Locate every Plasmodium parasite.
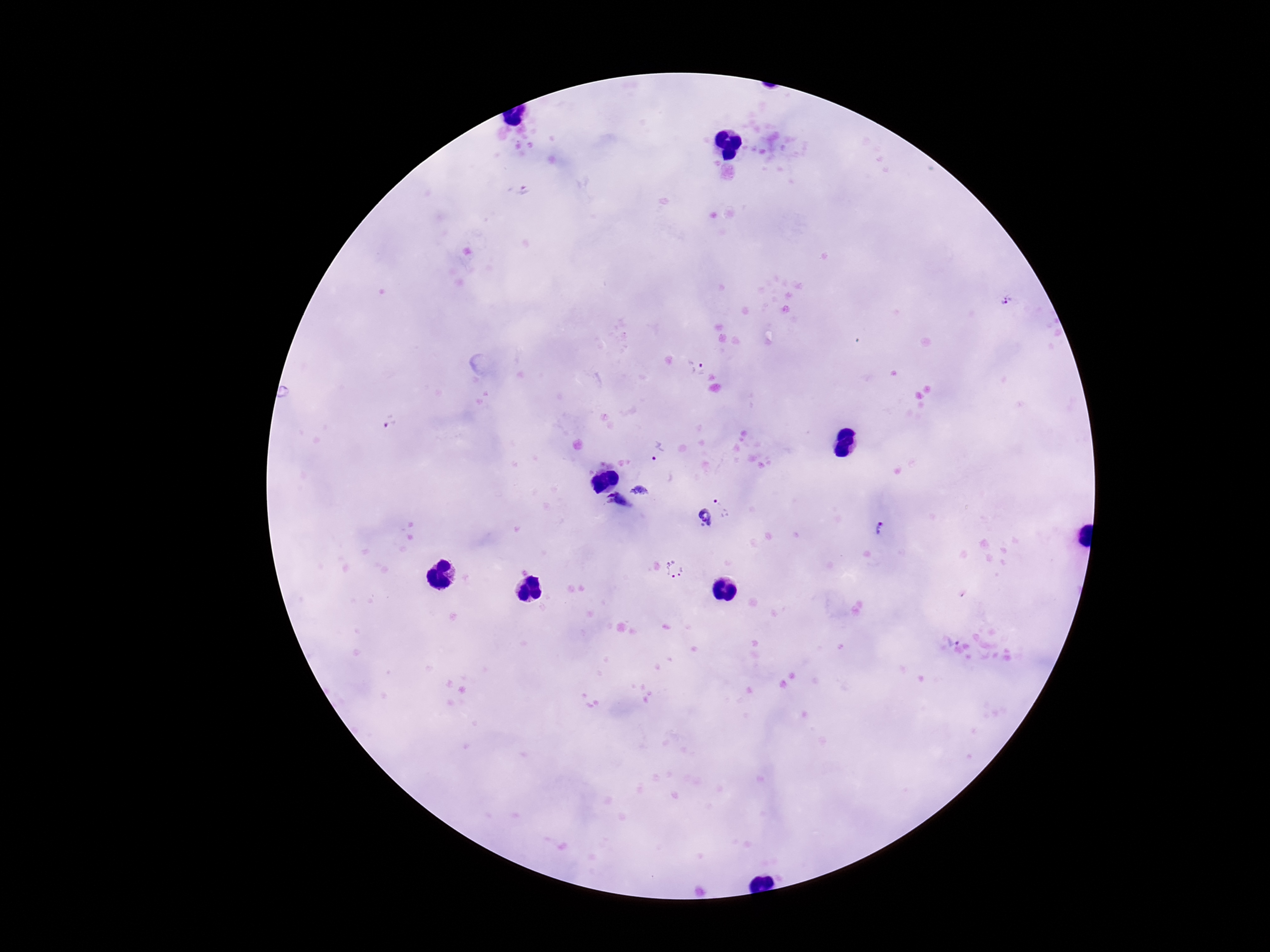

Approximate centers as {x, y} in pixels.
Plasmodium parasites: {523, 190}, {1007, 299}, {697, 368}, {389, 422}, {657, 451}, {727, 501}, {704, 520}, {881, 530}, {674, 569}, {951, 640}.

capture = smartphone camera through the microscope eyepiece
stain = Giemsa
preparation = thick peripheral-blood smear
magnification = 100x
field of view = one from this slide
image size = 1270×952 pixels
patient malaria status = infected